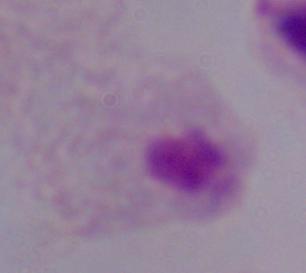
Summary:
  - Magnification: 1000x
  - Identification: trichomonad
  - Modality: micrograph